Mark where platelets are.
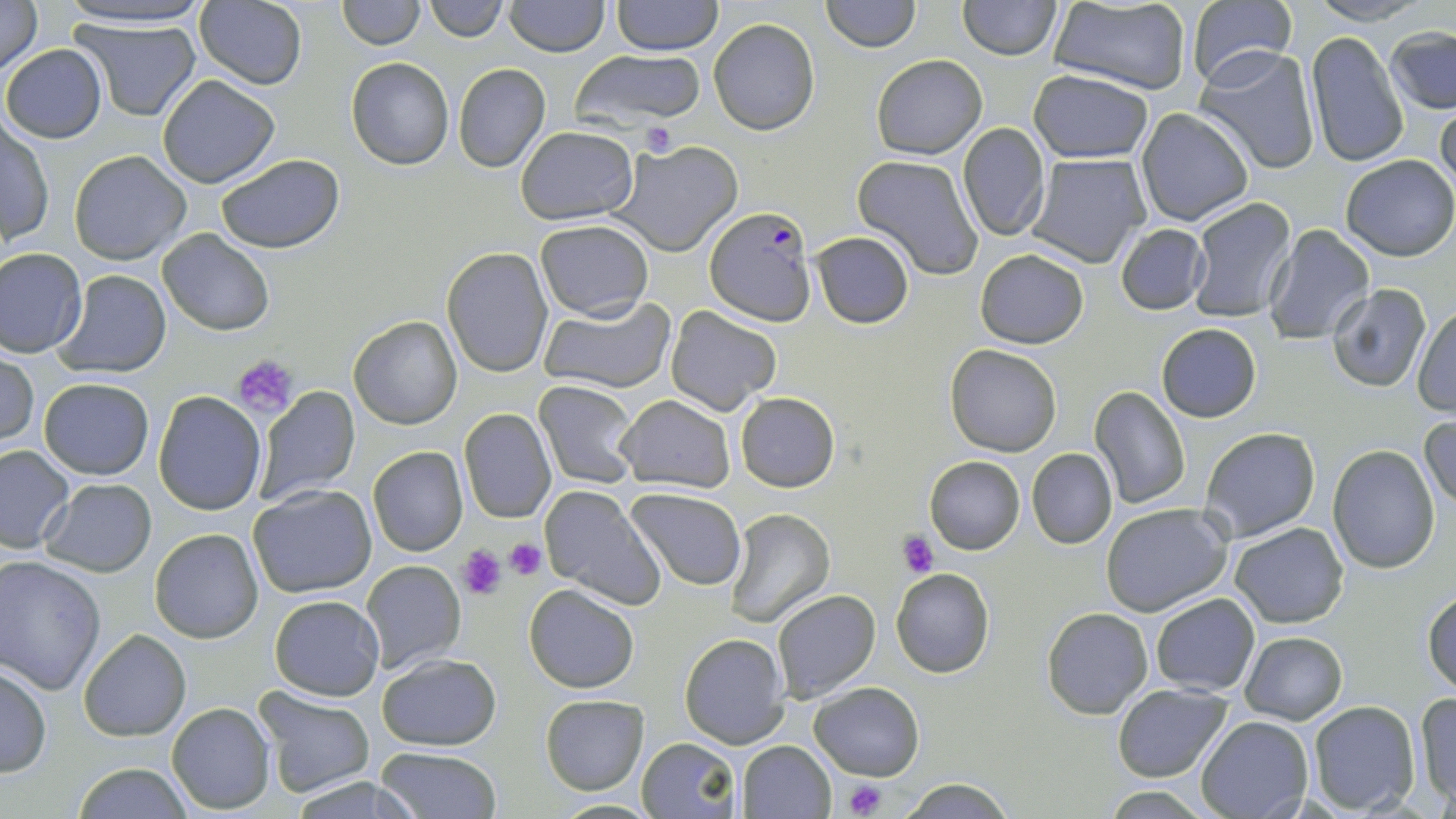
Approximate bounding boxes as (x1, y1, x2, y2) in pixels.
Platelets: (642, 122, 677, 156), (233, 354, 300, 418), (897, 532, 938, 578), (502, 537, 548, 581), (456, 544, 507, 599), (844, 779, 888, 817).

{
  "slide_level_diagnosis": "Plasmodium falciparum",
  "modality": "light microscopy",
  "image_size": "1456×819 pixels",
  "magnification": "1000x",
  "field_of_view": "single",
  "plasmodium_falciparum_infected_red_blood_cell_locations": "approximate bounding boxes as (x1, y1, x2, y2) in pixels: (705, 204, 817, 327)",
  "uninfected_red_blood_cell_locations": "approximate bounding boxes as (x1, y1, x2, y2) in pixels: (0, 0, 43, 79), (52, 0, 218, 32), (337, 0, 424, 48), (425, 0, 509, 43), (503, 0, 608, 56), (610, 0, 722, 55), (823, 0, 920, 52), (957, 0, 1061, 60), (1306, 0, 1432, 25), (194, 2, 308, 90), (1043, 2, 1194, 96), (1184, 2, 1299, 90), (70, 16, 202, 122), (708, 18, 820, 136), (1385, 25, 1454, 113), (1304, 31, 1409, 168), (2, 43, 107, 143), (1195, 46, 1322, 176), (570, 49, 709, 130), (871, 55, 987, 158), (346, 58, 454, 169), (453, 64, 551, 173), (1028, 69, 1154, 163), (156, 75, 281, 189), (1435, 103, 1456, 200), (1136, 107, 1253, 226), (1, 119, 53, 248), (958, 122, 1050, 242), (515, 126, 638, 224), (610, 139, 743, 256), (68, 149, 191, 266), (215, 152, 345, 254), (1026, 152, 1150, 269), (852, 155, 984, 279), (1339, 155, 1456, 259), (1185, 197, 1297, 324), (535, 218, 653, 320), (1116, 223, 1210, 315), (1262, 225, 1376, 345), (157, 229, 275, 336), (810, 231, 915, 328), (442, 247, 553, 377), (0, 248, 87, 358), (975, 250, 1089, 348), (54, 270, 171, 378), (1327, 285, 1432, 393), (539, 296, 676, 394), (665, 305, 781, 416), (1411, 306, 1456, 414), (349, 316, 463, 430), (1156, 324, 1262, 422), (945, 345, 1064, 457), (1, 350, 39, 450), (38, 378, 153, 481), (535, 380, 641, 488), (255, 386, 362, 504), (1088, 386, 1191, 511), (154, 391, 266, 516), (735, 392, 839, 492), (615, 395, 735, 491), (459, 408, 557, 524), (1421, 414, 1455, 515), (1199, 427, 1321, 542), (0, 444, 76, 554), (1330, 444, 1442, 575), (368, 446, 468, 557), (1027, 448, 1116, 549), (924, 456, 1027, 554), (39, 479, 157, 576), (247, 484, 378, 598), (539, 485, 662, 608), (625, 488, 747, 591), (1101, 501, 1233, 616), (723, 509, 834, 627), (1230, 521, 1350, 629), (149, 528, 264, 644), (0, 556, 105, 694), (361, 560, 466, 674), (890, 569, 995, 679), (524, 584, 639, 693), (1423, 587, 1456, 697), (771, 590, 881, 703), (1150, 593, 1260, 695), (269, 595, 384, 700), (1041, 608, 1153, 718), (79, 630, 192, 741), (1240, 632, 1347, 724), (679, 633, 789, 748), (376, 652, 503, 752), (0, 663, 51, 777), (810, 682, 924, 781), (1112, 683, 1234, 782), (256, 691, 376, 798), (1412, 692, 1455, 804), (540, 694, 648, 794), (1307, 700, 1420, 815), (166, 701, 276, 814), (1196, 715, 1313, 819), (638, 737, 740, 818), (736, 740, 834, 818), (373, 747, 503, 819), (69, 763, 197, 818), (291, 776, 421, 817), (900, 777, 1013, 817), (1103, 785, 1209, 817), (548, 799, 665, 817)",
  "stain": "May-Grünwald-Giemsa",
  "preparation": "thin blood smear"
}